State which parasite is depicted.
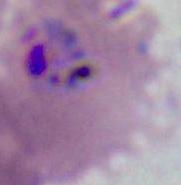
Plasmodium.

modality = micrograph
magnification = 400x or 1000x